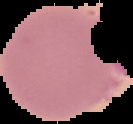
{
  "malaria_status": "uninfected",
  "image_size": "133×124 pixels",
  "image_type": "segmented cell region with the area outside set to black",
  "preparation": "thin blood smear"
}